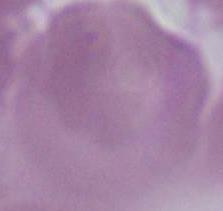

identification: erythrocyte
magnification: 1000x
modality: micrograph